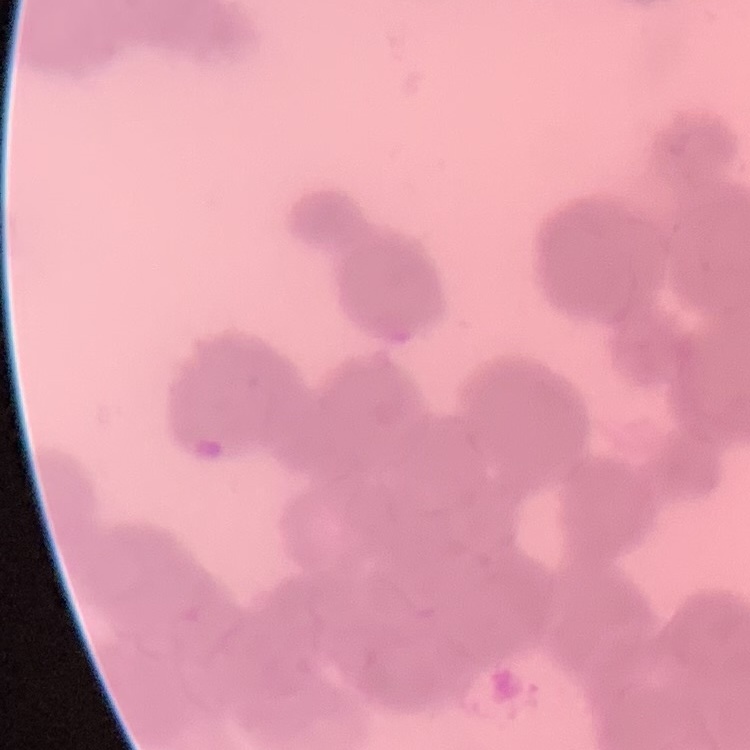

{
  "erythrocyte_morphology": "rouleaux formation",
  "preparation": "thin peripheral smear",
  "image_type": "square crop of a larger photomicrograph",
  "stain": "Field's or Giemsa"
}